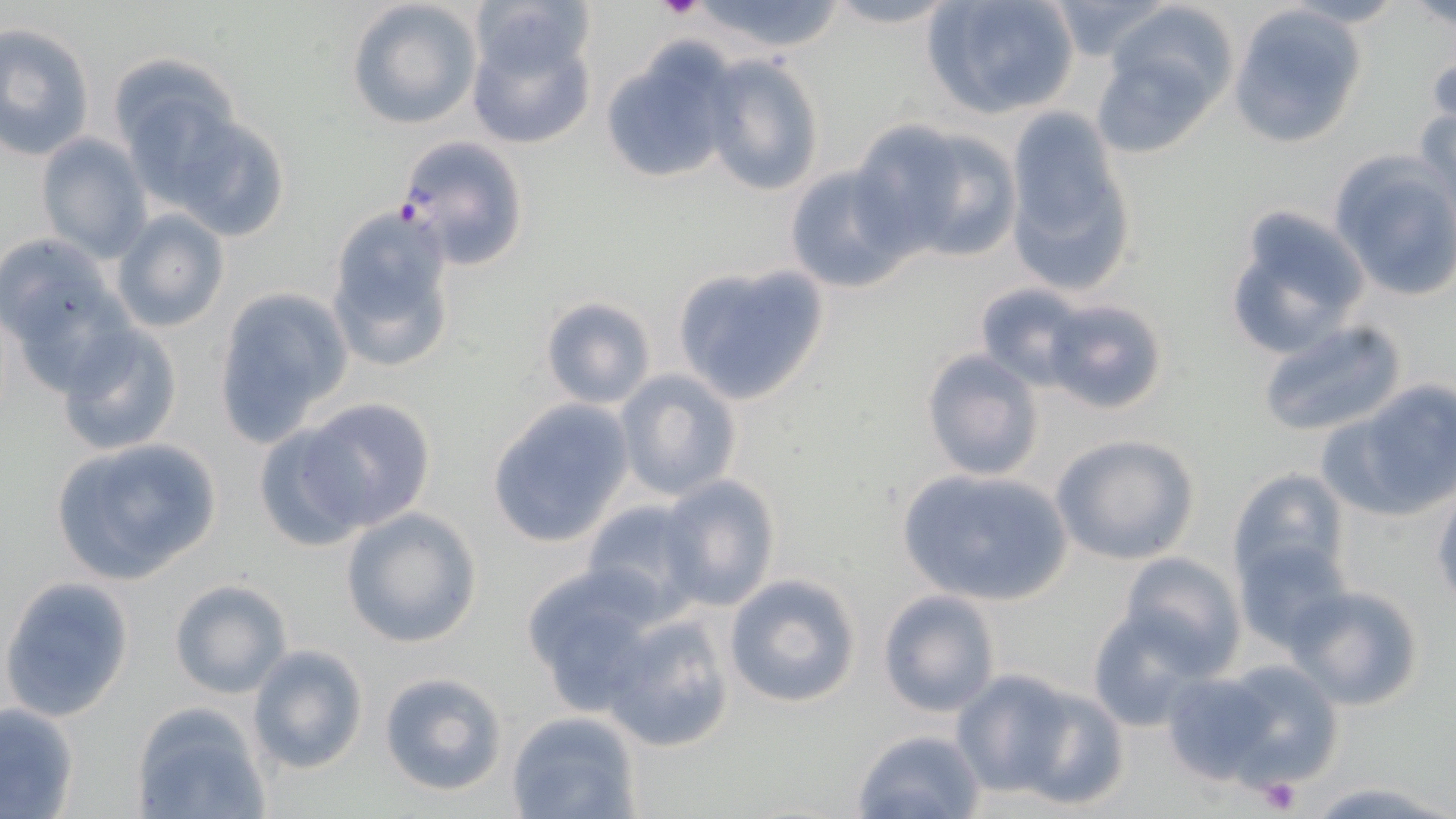
slide-level diagnosis = Plasmodium falciparum
modality = light microscopy
platelet locations = approximate bounding boxes as (x1, y1, x2, y2) in pixels: (655, 0, 701, 19), (1258, 776, 1302, 815)
image size = 1456×819 pixels
stain = May-Grünwald-Giemsa
uninfected red blood cell locations = approximate bounding boxes as (x1, y1, x2, y2) in pixels: (346, 0, 483, 130), (689, 0, 848, 55), (922, 0, 1082, 121), (1406, 0, 1456, 29), (819, 1, 961, 30), (1102, 1, 1241, 120), (1048, 2, 1176, 63), (1230, 4, 1367, 148), (466, 13, 596, 151), (0, 22, 95, 159), (597, 40, 741, 186), (1088, 47, 1220, 159), (700, 54, 826, 197), (109, 60, 241, 193), (1413, 103, 1455, 211), (1005, 106, 1134, 286), (172, 114, 292, 242), (853, 119, 1011, 261), (36, 132, 152, 260), (1330, 155, 1456, 300), (784, 164, 916, 295), (323, 204, 462, 376), (1224, 206, 1369, 359), (111, 208, 230, 334), (0, 233, 120, 355), (671, 265, 829, 406), (975, 281, 1090, 389), (211, 286, 352, 441), (540, 295, 656, 409), (1046, 295, 1168, 415), (1255, 319, 1407, 442), (56, 323, 183, 456), (918, 349, 1045, 482), (616, 370, 742, 500), (1346, 381, 1455, 513), (303, 397, 435, 531), (486, 399, 634, 546), (324, 412, 465, 621), (252, 420, 372, 552), (1050, 434, 1200, 566), (51, 436, 222, 584), (895, 467, 1073, 604), (1227, 467, 1350, 586), (657, 475, 780, 611), (1431, 490, 1456, 608), (581, 498, 706, 617), (339, 508, 483, 648), (1234, 538, 1352, 652), (1118, 550, 1244, 673), (519, 564, 667, 712), (722, 573, 860, 709), (0, 575, 134, 723), (167, 577, 293, 698), (1289, 584, 1425, 710), (877, 589, 1002, 717), (1087, 608, 1215, 733), (605, 614, 735, 752), (246, 643, 369, 774), (1214, 658, 1343, 788), (951, 670, 1075, 796), (377, 671, 508, 796), (1163, 671, 1277, 782), (1008, 684, 1130, 807), (0, 701, 79, 818), (133, 704, 270, 818), (505, 711, 640, 819), (850, 727, 985, 819), (1306, 780, 1451, 819)
magnification = 1000x
preparation = thin blood smear
field of view = one of a larger specimen
Plasmodium falciparum-infected red blood cell locations = approximate bounding boxes as (x1, y1, x2, y2) in pixels: (394, 133, 529, 270)